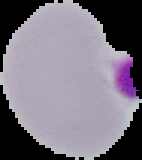
malaria status = uninfected
image type = segmented cell region on a black background
preparation = thin blood smear
image size = 142×160 pixels